Classify this cell by malaria status.
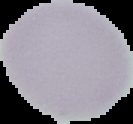
Uninfected.

preparation: thin blood film
image_size: 133×124 pixels
image_type: segmented cell region on a black background